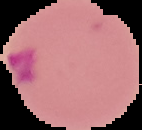
Image is 142×130 pixels. From a thin blood film. Cell region segmented out of the field of view; the surrounding area is masked to black. Result: malaria parasites detected.